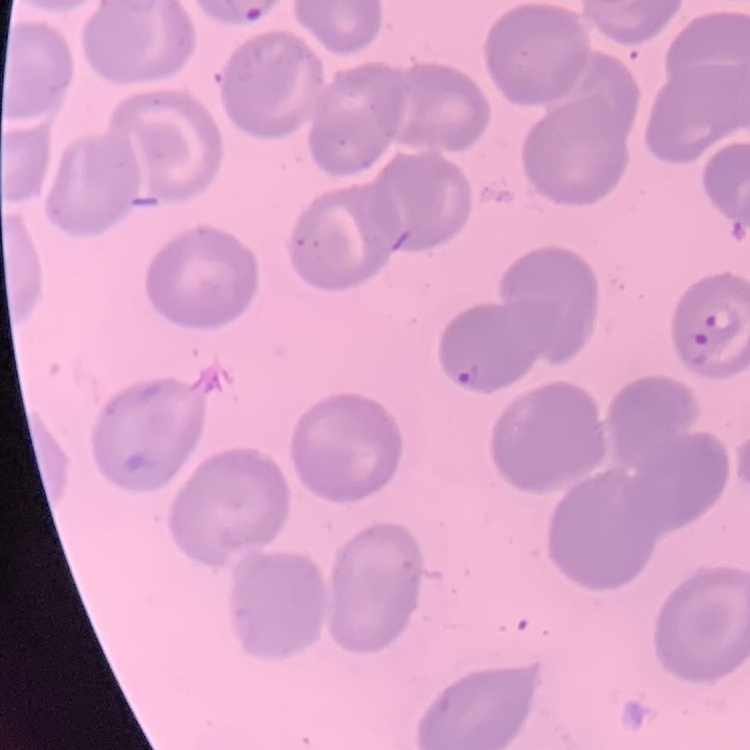

The red blood cells exhibit no rouleaux formation. One tile cut from a larger photomicrograph. Field's or Giemsa stain. Thin peripheral smear.